Give the position of every malaria parasite.
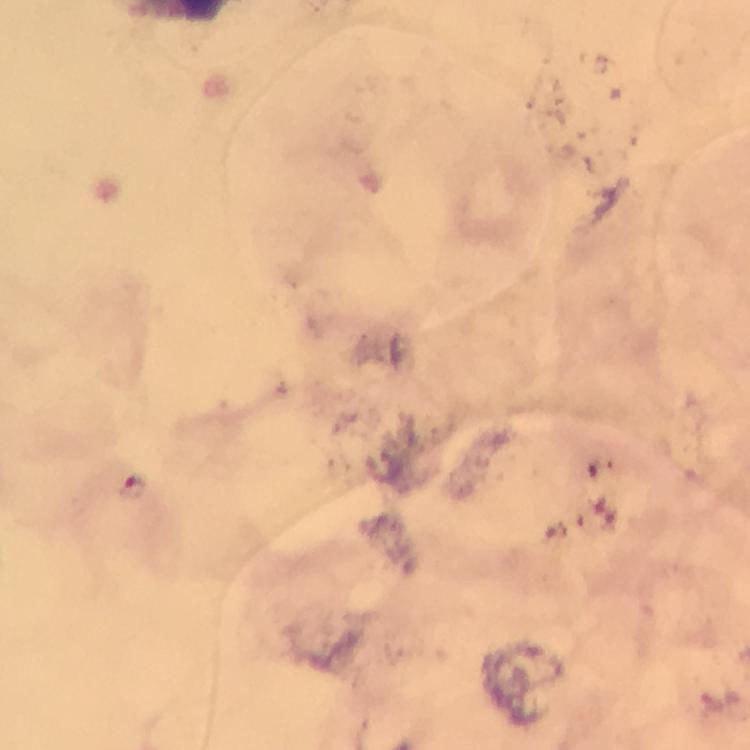

Approximate object centers, in pixels from the top-left corner.
Malaria parasites: (x=135, y=491).

capture: smartphone camera through the microscope
image_size: 750×750 pixels
cropped_from: a single field of view
magnification: 100x
preparation: thick smear
immersion_oil: applied
stain: Giemsa
context: from a malaria diagnostic workup